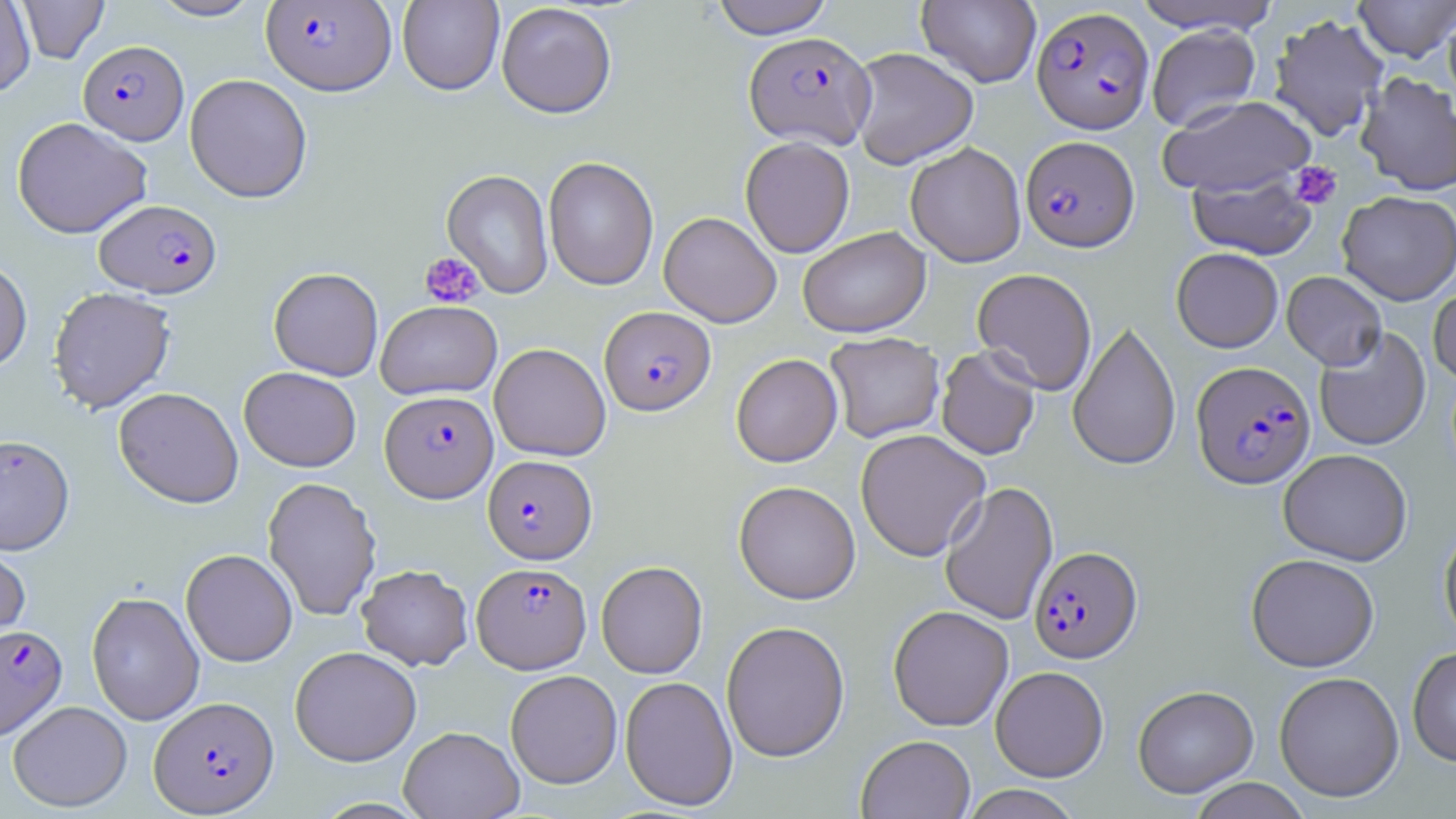
plasmodium_falciparum_infected_red_blood_cell_locations: 'approximate bounding boxes as [x1, y1, x2, y2] in pixels: [261, 1, 396, 95], [1032, 6, 1154, 134], [744, 31, 875, 149], [78, 40, 189, 144], [1020, 135, 1139, 252], [94, 199, 221, 298], [600, 306, 716, 415], [1191, 360, 1315, 489], [381, 390, 499, 502], [0, 434, 75, 555], [483, 455, 597, 564], [1029, 546, 1142, 663], [472, 562, 591, 673], [0, 624, 68, 742], [149, 695, 279, 816]'
slide_level_diagnosis: Plasmodium falciparum
magnification: 1000x
stain: May-Grünwald-Giemsa
uninfected_red_blood_cell_locations: 'approximate bounding boxes as [x1, y1, x2, y2] in pixels: [0, 0, 36, 96], [16, 0, 110, 65], [147, 0, 264, 21], [710, 0, 834, 39], [916, 0, 1042, 87], [1130, 0, 1282, 34], [1354, 0, 1456, 62], [397, 1, 504, 96], [496, 2, 617, 118], [1443, 4, 1456, 108], [1268, 13, 1389, 142], [1147, 24, 1261, 131], [848, 46, 979, 169], [1356, 70, 1456, 196], [185, 73, 312, 203], [1158, 95, 1318, 197], [12, 117, 152, 239], [740, 136, 855, 258], [905, 142, 1027, 267], [543, 156, 659, 290], [441, 169, 554, 299], [1187, 170, 1318, 261], [1337, 191, 1456, 305], [659, 211, 781, 327], [798, 227, 931, 338], [1171, 247, 1283, 353], [0, 258, 33, 374], [268, 267, 383, 381], [972, 268, 1097, 395], [1282, 271, 1387, 370], [1428, 281, 1456, 386], [48, 286, 176, 413], [376, 300, 501, 400], [1067, 320, 1181, 471], [1314, 327, 1431, 452], [825, 332, 944, 443], [489, 343, 611, 461], [935, 346, 1041, 460], [731, 353, 842, 467], [239, 366, 361, 471], [113, 387, 244, 508], [855, 428, 991, 561], [1278, 449, 1412, 565], [262, 476, 381, 621], [733, 480, 861, 604], [939, 481, 1058, 625], [1438, 521, 1456, 646], [0, 534, 32, 657], [181, 548, 298, 667], [1246, 553, 1379, 672], [596, 561, 707, 678], [357, 564, 473, 670], [86, 591, 205, 725], [888, 605, 1014, 731], [721, 620, 850, 762], [289, 646, 422, 766], [1407, 646, 1456, 767], [991, 666, 1108, 782], [505, 670, 622, 789], [1273, 671, 1404, 802], [620, 676, 738, 811], [1132, 685, 1259, 798], [8, 700, 132, 812], [398, 726, 524, 818], [856, 734, 975, 819], [1188, 778, 1311, 818], [960, 784, 1082, 819]'
modality: optical microscopy
field_of_view: one of a larger specimen
image_size: 1456×819 pixels
preparation: thin blood film
platelet_locations: 'approximate bounding boxes as [x1, y1, x2, y2] in pixels: [1289, 162, 1342, 209], [418, 251, 485, 309]'